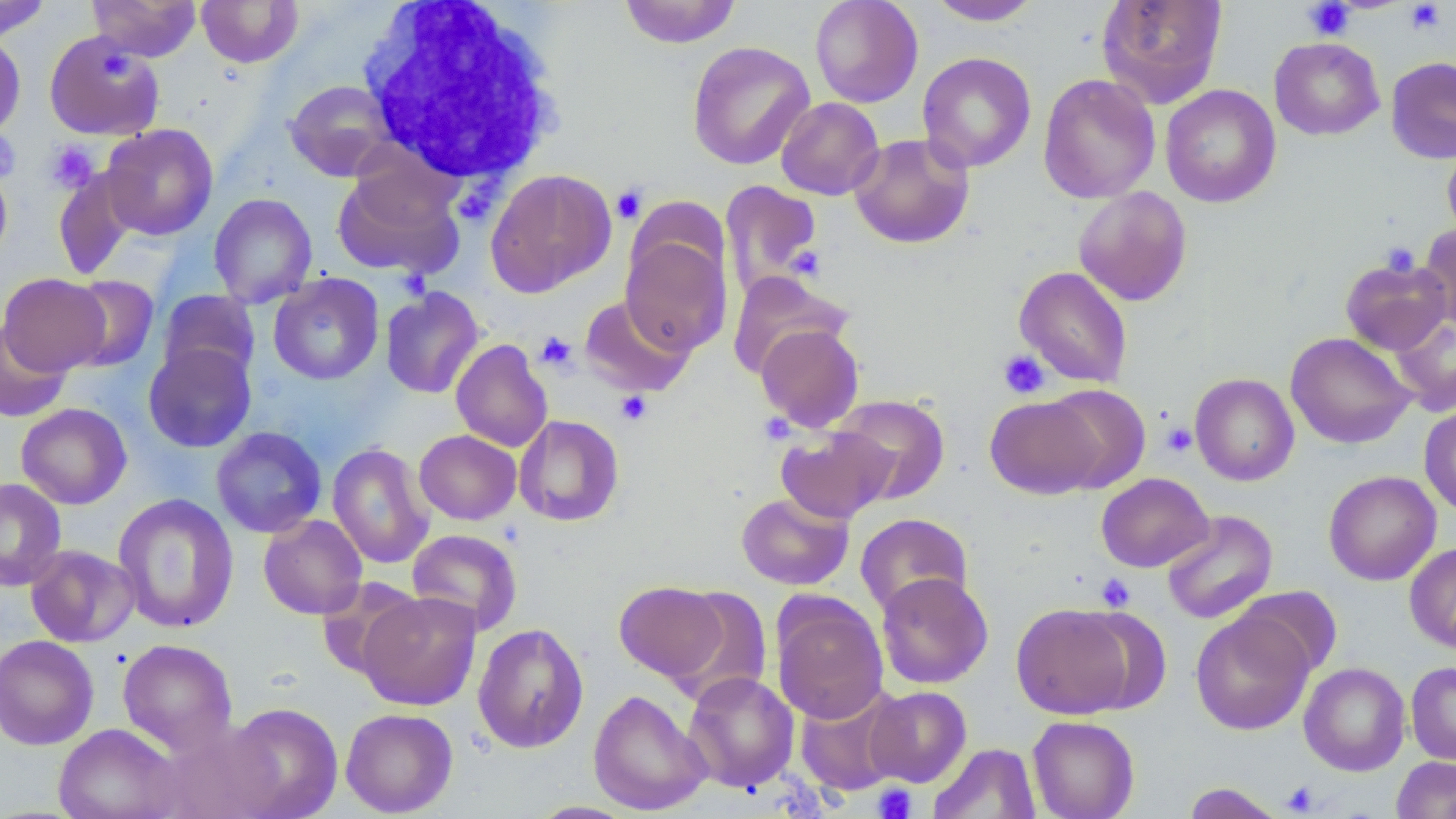 Approximate bounding boxes as (x1,y1)-(x2,y2) corner pairs in pixels. Platelet locations: (1303,0)-(1355,40), (1404,1)-(1445,34), (101,52)-(133,80), (0,129)-(21,182), (44,140)-(100,193), (611,185)-(647,223), (1380,242)-(1420,277), (786,244)-(825,280), (535,331)-(578,372), (998,349)-(1050,399), (616,391)-(652,425), (1161,423)-(1196,457), (1096,573)-(1135,612), (1281,782)-(1319,815), (873,783)-(917,819). White blood cell locations: (358,0)-(565,186). Uninfected red blood cell locations: (88,0)-(201,61), (196,0)-(304,68), (617,0)-(742,49), (809,0)-(924,108), (926,0)-(1043,26), (1096,0)-(1228,108), (0,1)-(52,42), (43,30)-(166,141), (0,32)-(26,140), (1269,37)-(1384,140), (687,41)-(815,170), (917,51)-(1036,173), (1385,56)-(1456,164), (1038,73)-(1161,203), (284,79)-(398,181), (1160,84)-(1281,208), (775,97)-(885,200), (100,123)-(219,241), (849,133)-(975,249), (1442,143)-(1456,243), (332,163)-(464,280), (0,165)-(12,267), (52,167)-(139,281), (485,168)-(616,297), (720,181)-(822,298), (1073,187)-(1192,306), (209,193)-(317,308), (1418,224)-(1456,330), (621,233)-(732,355), (1340,256)-(1451,355), (1013,266)-(1133,388), (727,270)-(852,379), (0,273)-(110,375), (64,274)-(160,372), (268,274)-(384,384), (380,287)-(484,399), (158,289)-(260,384), (579,294)-(696,398), (1389,313)-(1456,416), (0,320)-(71,422), (755,322)-(865,432), (1286,332)-(1415,448), (451,339)-(552,452), (143,343)-(256,452), (1189,373)-(1299,486), (1042,384)-(1150,493), (832,394)-(951,504), (985,395)-(1104,499), (16,403)-(132,509), (1419,404)-(1456,517), (514,414)-(624,527), (211,426)-(327,538), (775,426)-(897,523), (414,430)-(521,525), (327,443)-(434,569), (1323,470)-(1441,586), (1096,472)-(1213,572), (0,478)-(67,591), (736,492)-(854,590), (113,493)-(239,634), (1160,510)-(1278,625), (855,512)-(973,617), (259,514)-(367,619), (407,529)-(523,636), (1404,543)-(1456,654), (25,544)-(140,647), (876,571)-(993,689), (317,577)-(424,682), (614,581)-(728,683), (665,585)-(773,705), (1235,585)-(1342,678), (357,589)-(482,711), (771,594)-(888,724), (1011,602)-(1136,719), (1072,606)-(1172,714), (1191,610)-(1314,735), (472,623)-(589,753), (0,634)-(99,751), (117,638)-(238,754), (1406,661)-(1456,765), (1299,662)-(1410,775), (684,671)-(800,792), (794,685)-(907,797), (865,686)-(972,787), (588,688)-(711,815), (223,702)-(343,818), (340,708)-(458,816), (1027,715)-(1140,819), (160,718)-(286,819), (53,723)-(184,819), (928,743)-(1040,818), (1391,756)-(1456,818), (1182,782)-(1287,819). Slide-level diagnosis: no evidence of blood parasites. One field of a larger specimen. Image is 1456×819 pixels. Optical microscopy. May-Grünwald-Giemsa-stained preparation. 1000x magnification. Thin blood film.